Outline each blood parasite and name the species.
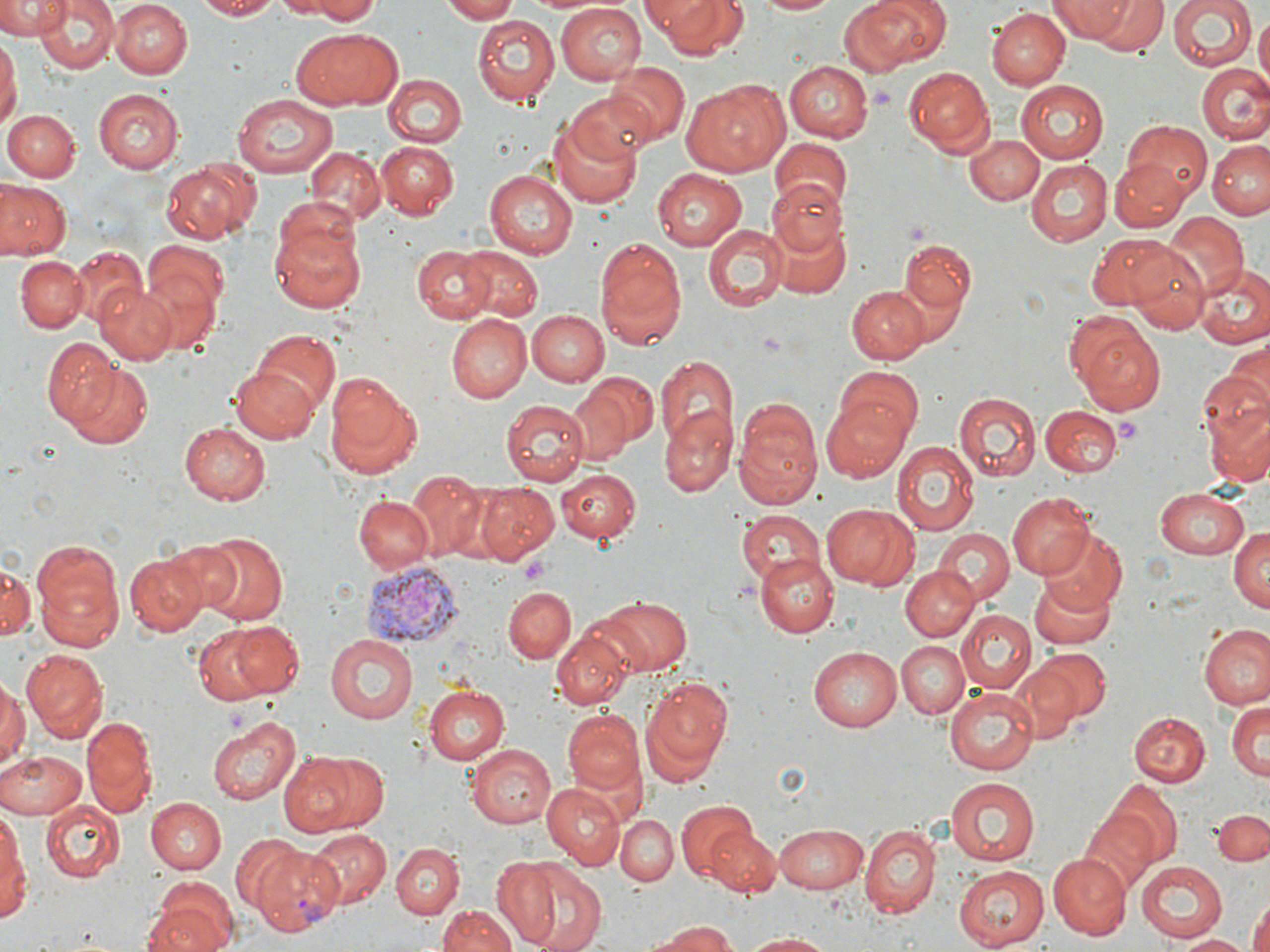

Approximate bounding boxes as (x1, y1, x2, y2) in pixels.
Plasmodium vivax-infected red blood cells: (359, 561, 456, 646), (248, 841, 343, 936).
No Plasmodium falciparum, Plasmodium ovale, Plasmodium malariae, Babesia divergens, or Trypanosoma brucei observed.

Summary:
  - Platelet locations: (1114, 417, 1141, 445), (520, 559, 550, 585)
  - Uninfected red blood cell locations: (0, 0, 69, 38), (109, 0, 192, 78), (191, 0, 280, 20), (295, 0, 382, 22), (442, 0, 522, 22), (641, 0, 750, 60), (754, 0, 839, 16), (848, 0, 943, 71), (1061, 0, 1169, 57), (1167, 2, 1258, 73), (35, 3, 117, 74), (556, 5, 645, 84), (987, 8, 1068, 90), (1253, 12, 1269, 87), (472, 14, 561, 107), (292, 28, 401, 110), (0, 37, 19, 133), (784, 60, 873, 141), (610, 61, 689, 146), (1197, 63, 1268, 144), (903, 66, 994, 155), (382, 75, 463, 147), (1016, 78, 1113, 162), (682, 79, 790, 176), (565, 88, 659, 166), (93, 89, 182, 172), (232, 94, 337, 179), (3, 109, 79, 182), (550, 118, 643, 205), (1118, 119, 1212, 208), (967, 134, 1044, 205), (768, 137, 853, 213), (1209, 140, 1270, 221), (378, 141, 459, 216), (303, 147, 385, 227), (161, 158, 259, 241), (1026, 158, 1113, 244), (1112, 161, 1188, 232), (653, 168, 745, 252), (484, 171, 578, 259), (0, 180, 71, 260), (766, 180, 846, 257), (1157, 213, 1247, 301), (266, 214, 368, 314), (771, 219, 850, 300), (704, 225, 785, 310), (1090, 232, 1187, 311), (594, 234, 688, 349), (142, 238, 229, 340), (902, 241, 975, 313), (411, 244, 496, 323), (455, 246, 543, 323), (1126, 246, 1211, 335), (70, 248, 146, 325), (14, 256, 88, 332), (1190, 266, 1270, 347), (95, 282, 177, 365), (849, 285, 931, 363), (525, 309, 607, 387), (1065, 310, 1167, 416), (447, 313, 530, 402), (252, 331, 339, 419), (43, 337, 121, 426), (1227, 341, 1269, 413), (657, 356, 736, 448), (64, 361, 153, 448), (232, 364, 322, 442), (835, 368, 925, 453), (322, 369, 425, 479), (581, 372, 658, 453), (1200, 372, 1269, 489), (563, 384, 635, 466), (954, 391, 1040, 483), (819, 394, 915, 480), (733, 398, 822, 509), (501, 399, 589, 484), (1040, 404, 1121, 476), (661, 407, 737, 497), (179, 423, 269, 505), (893, 440, 979, 534), (554, 467, 641, 545), (407, 472, 492, 557), (473, 481, 561, 562), (1154, 489, 1250, 560), (1007, 491, 1098, 579), (353, 495, 433, 572), (823, 503, 918, 591), (737, 509, 824, 586), (1229, 523, 1270, 616), (1040, 527, 1128, 614), (933, 528, 1015, 606), (199, 531, 288, 627), (156, 537, 245, 617), (31, 539, 125, 648), (127, 552, 207, 637), (754, 552, 837, 637), (2, 559, 36, 640), (901, 566, 979, 641), (1031, 571, 1117, 649), (504, 586, 576, 663), (588, 593, 694, 675), (956, 612, 1034, 693), (190, 621, 298, 706), (1198, 624, 1269, 709), (551, 628, 631, 709), (325, 634, 418, 723), (896, 640, 968, 718), (809, 644, 906, 732), (23, 649, 107, 738), (1029, 649, 1110, 725), (1011, 660, 1087, 739), (0, 676, 25, 774), (642, 676, 734, 773), (422, 684, 510, 766), (946, 687, 1039, 776), (1226, 700, 1269, 782), (564, 711, 647, 797), (1128, 711, 1208, 787), (206, 716, 304, 804), (81, 718, 155, 816), (467, 744, 556, 829), (0, 748, 88, 818), (283, 749, 385, 833), (943, 776, 1041, 867), (1106, 781, 1182, 864), (541, 782, 625, 870), (146, 797, 225, 874), (675, 801, 763, 885), (43, 802, 124, 882), (0, 806, 28, 923), (1214, 809, 1269, 865), (1078, 810, 1158, 894), (615, 813, 679, 887), (772, 823, 869, 893), (860, 823, 939, 916), (709, 828, 783, 896), (305, 829, 391, 908), (231, 835, 306, 920), (389, 843, 461, 918), (1048, 852, 1130, 940), (487, 856, 577, 947), (1136, 861, 1229, 941), (517, 864, 607, 952), (955, 866, 1050, 949), (144, 880, 239, 952), (1249, 898, 1269, 952), (436, 902, 518, 952), (650, 919, 736, 951), (742, 933, 837, 952), (1179, 933, 1251, 951)
  - Slide-level diagnosis: Plasmodium vivax
  - Field of view: single
  - Image size: 1270×952 pixels
  - Preparation: thin blood film
  - Magnification: 1000x
  - Stain: May-Grünwald-Giemsa
  - Modality: light microscopy